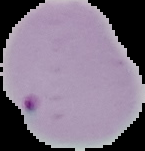

Segmented cell region on a black background. Malaria status: parasitized. Image is 145×151 pixels. From a thin blood film.